Look for Plasmodium parasites.
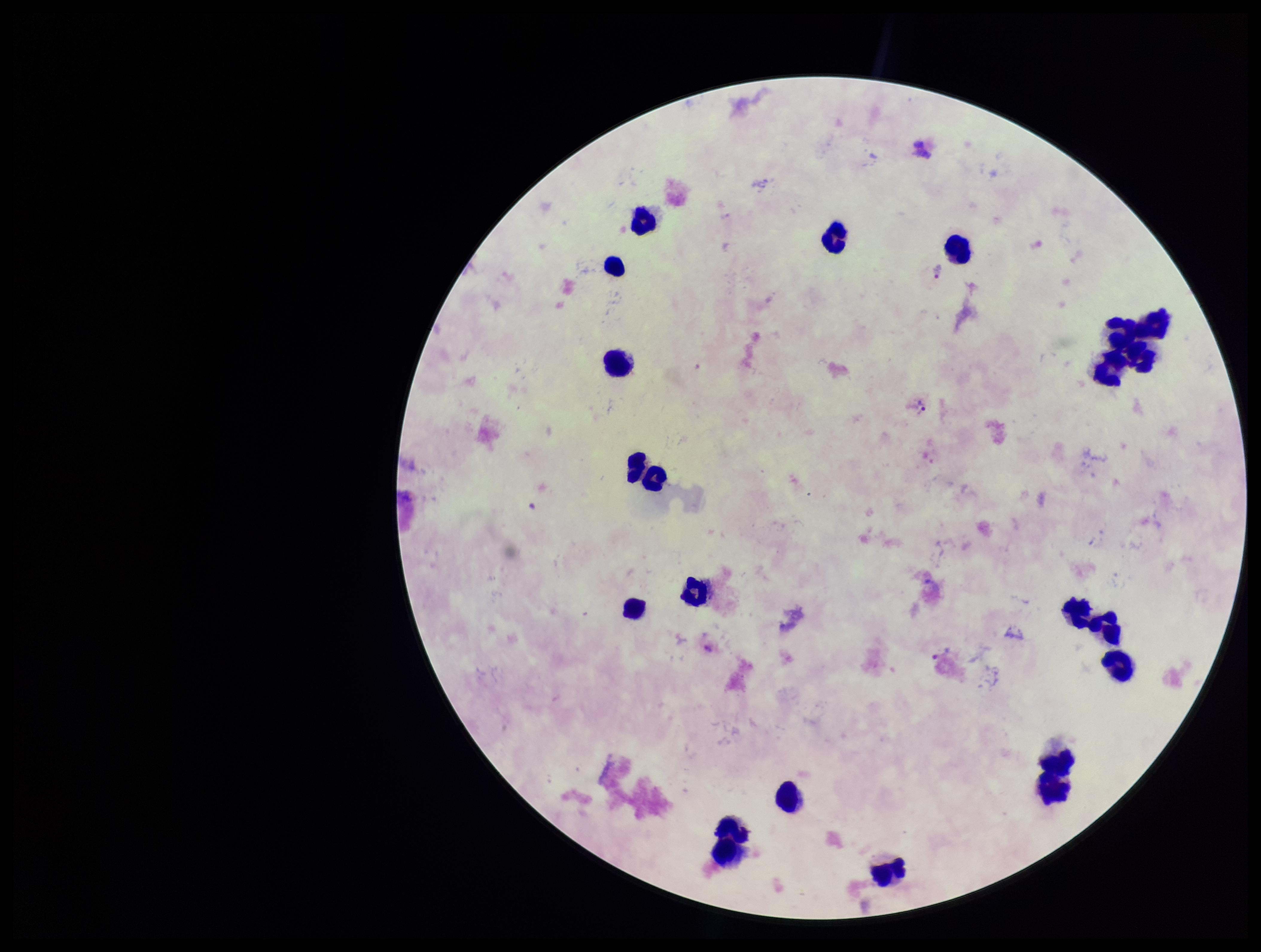
Detected.

preparation = thick
stain = Giemsa
field of view = single
patient malaria status = infected
species reported for this patient = Plasmodium vivax
parasite count = 4
capture = smartphone photograph through the microscope eyepiece
image size = 1261×952 pixels
leukocyte count = 20